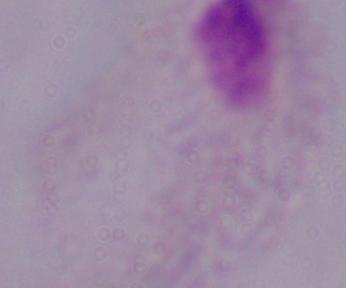
Summary:
  - Magnification: 1000x
  - Modality: photomicrograph
  - Identification: trichomonad